Report the malaria status of this cell.
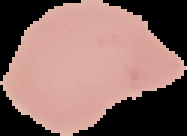
It is uninfected.

{
  "image_size": "187×136 pixels",
  "preparation": "thin blood smear",
  "image_type": "segmented cell region with the area outside set to black"
}